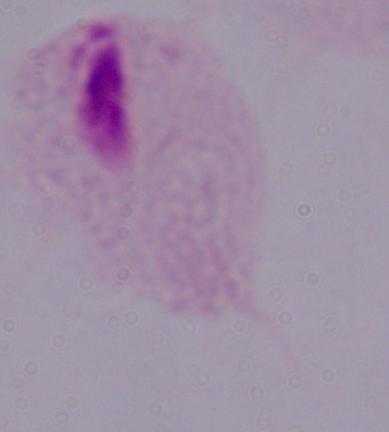
modality = micrograph
identification = trichomonad
magnification = 1000x